Name the parasite shown.
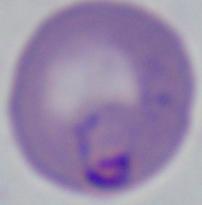
Babesia.

Summary:
  - Magnification: 1000x
  - Modality: micrograph